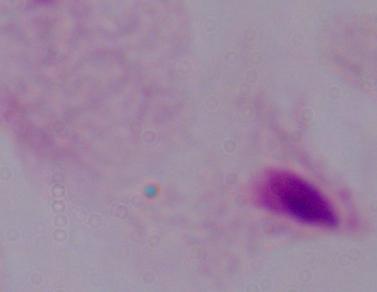
1000x magnification. Micrograph. A trichomonad is shown.